Locate and identify every blood parasite.
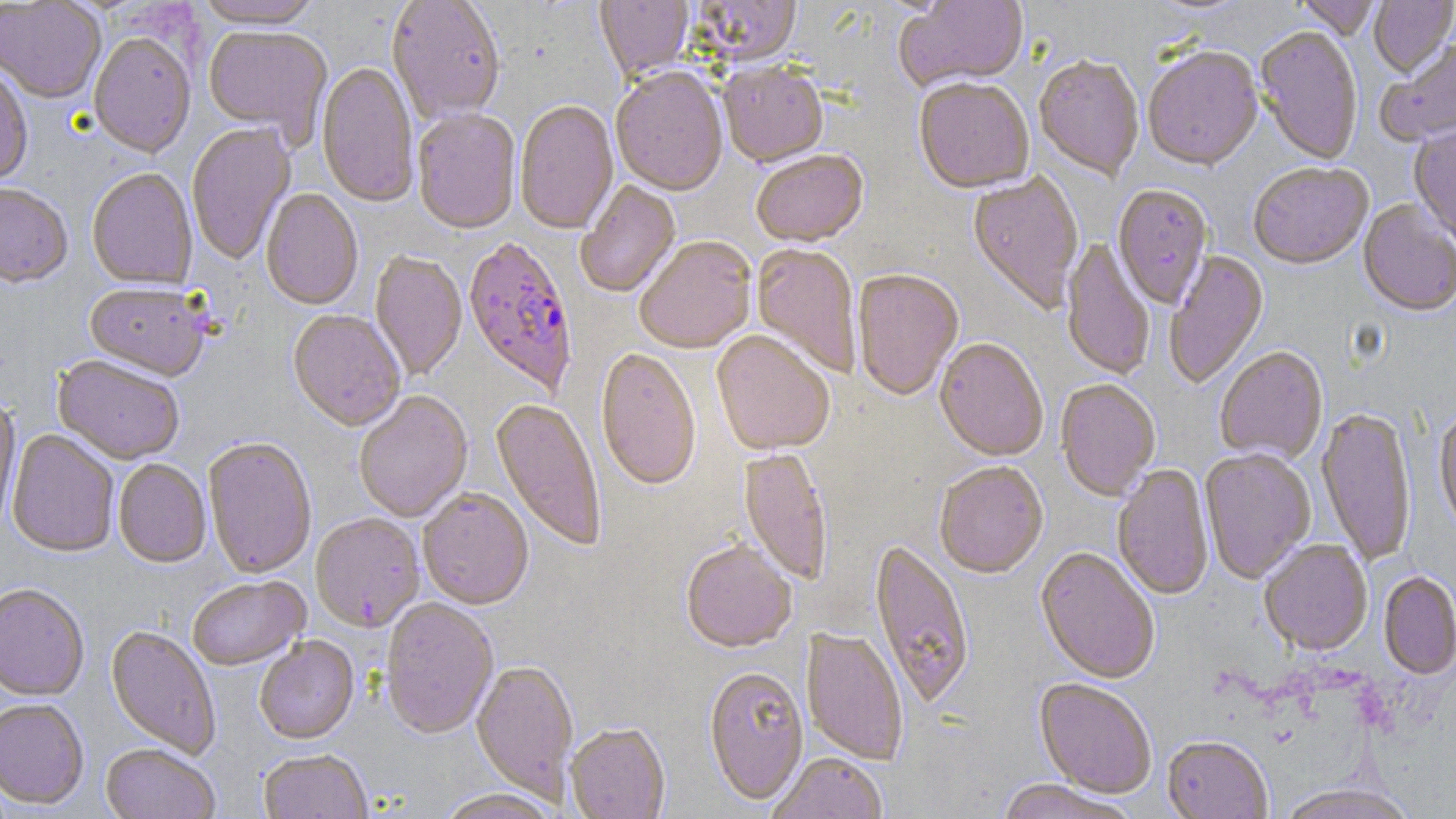

Approximate bounding boxes as (x1,y1)-(x2,y2) corner pairs in pixels.
Plasmodium falciparum-infected red blood cells: (462,239)-(578,398).
No Plasmodium ovale, Plasmodium malariae, Plasmodium vivax, Babesia divergens, or Trypanosoma brucei observed.

Uninfected red blood cell locations: (194,0)-(322,31), (387,0)-(505,125), (595,0)-(694,81), (895,0)-(1030,93), (1145,0)-(1251,16), (1295,0)-(1381,42), (1369,0)-(1456,79), (0,1)-(106,105), (688,1)-(802,68), (203,26)-(332,147), (1254,27)-(1363,166), (88,33)-(196,161), (1377,39)-(1456,148), (1142,49)-(1263,173), (1033,58)-(1144,182), (316,62)-(419,210), (718,64)-(828,170), (1,65)-(34,188), (610,69)-(728,199), (914,80)-(1034,196), (514,100)-(620,237), (412,111)-(521,237), (186,123)-(297,265), (1408,124)-(1456,246), (752,152)-(869,249), (1249,164)-(1373,272), (86,169)-(198,292), (968,172)-(1084,316), (575,181)-(681,299), (0,185)-(72,291), (1112,186)-(1213,310), (261,190)-(363,311), (1357,201)-(1456,318), (635,238)-(756,355), (1060,240)-(1154,382), (751,245)-(861,378), (1164,251)-(1270,390), (370,252)-(467,382), (852,270)-(964,402), (84,284)-(209,383), (287,311)-(405,433), (711,332)-(834,457), (934,341)-(1048,463), (1214,348)-(1328,466), (595,350)-(701,493), (53,357)-(184,467), (1056,381)-(1160,502), (354,392)-(473,523), (0,397)-(21,539), (489,399)-(606,552), (1316,408)-(1417,568), (1434,409)-(1456,543), (6,429)-(119,559), (203,438)-(317,580), (739,449)-(832,587), (1200,449)-(1316,585), (114,460)-(211,570), (934,463)-(1048,581), (1112,466)-(1214,601), (418,490)-(534,611), (311,514)-(425,634), (869,541)-(975,711), (1258,541)-(1373,657), (681,543)-(796,655), (1035,549)-(1159,685), (1378,572)-(1456,681), (188,578)-(310,672), (0,585)-(89,702), (380,600)-(498,740), (105,626)-(221,759), (800,628)-(908,766), (255,637)-(360,746), (471,661)-(579,804), (703,668)-(810,808), (1033,679)-(1156,799), (0,700)-(89,811), (566,725)-(670,819), (1162,737)-(1273,819), (100,745)-(219,819), (259,751)-(373,819), (767,755)-(887,819), (995,780)-(1137,819), (1273,785)-(1421,819), (436,790)-(560,819). Slide-level diagnosis: Plasmodium falciparum. Optical microscopy. May-Grünwald-Giemsa-stained preparation. Image is 1456×819 pixels. Thin blood film. One field of a larger specimen. Captured at 1000x magnification.